Comment on the morphology of the erythrocytes.
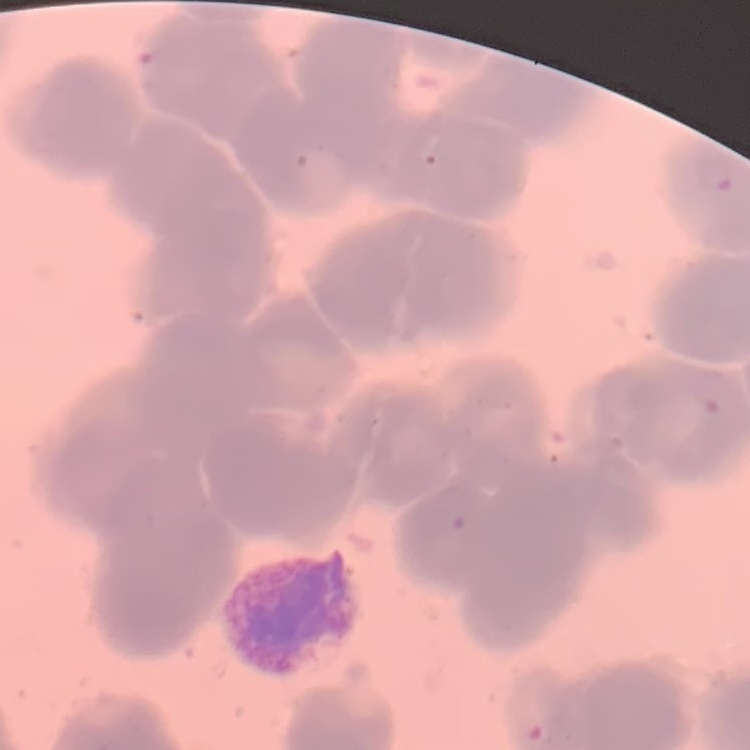

Rouleaux formation.

preparation = thin blood film
stain = Field's or Giemsa
image type = one tile cut from a larger photomicrograph